State which parasite is depicted.
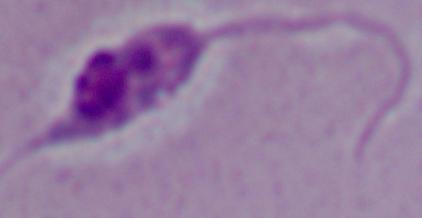
This is Leishmania.

magnification: 1000x
modality: photomicrograph